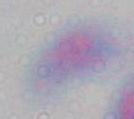
{
  "identification": "Toxoplasma gondii",
  "magnification": "1000x",
  "modality": "micrograph"
}